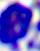

{
  "modality": "micrograph",
  "magnification": "400x",
  "identification": "leukocyte"
}